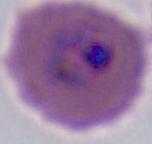

400x or 1000x magnification. Photomicrograph. A Plasmodium parasite is shown.